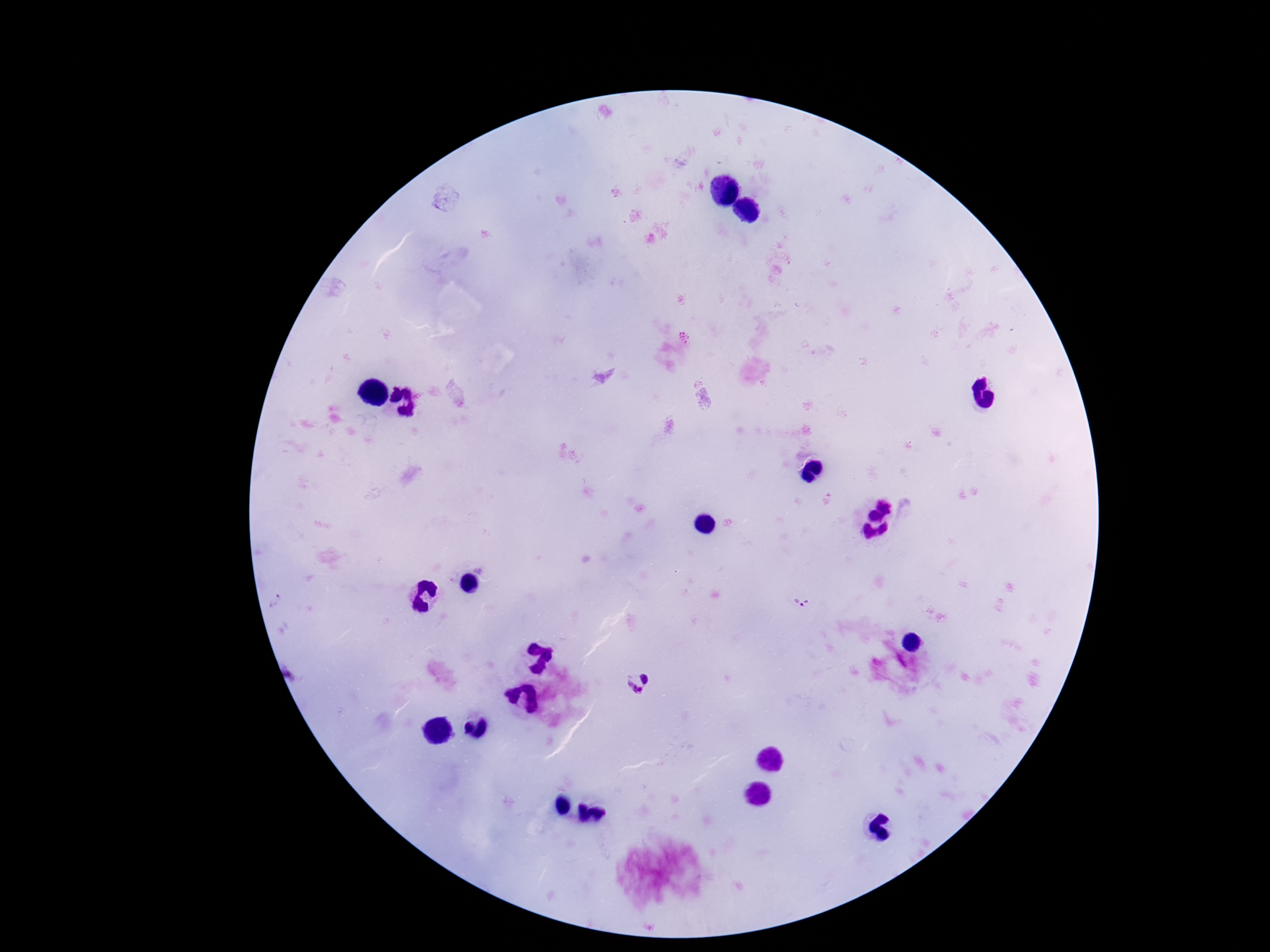
Approximate centers as {x, y} in pixels. Plasmodium parasite locations: {803, 600}, {645, 678}, {632, 691}. 100x magnification. Single field of view. Image is 1270×952 pixels. Thick peripheral-blood smear. Giemsa-stained preparation. Smartphone photograph taken through the microscope eyepiece. Patient malaria status: positive.